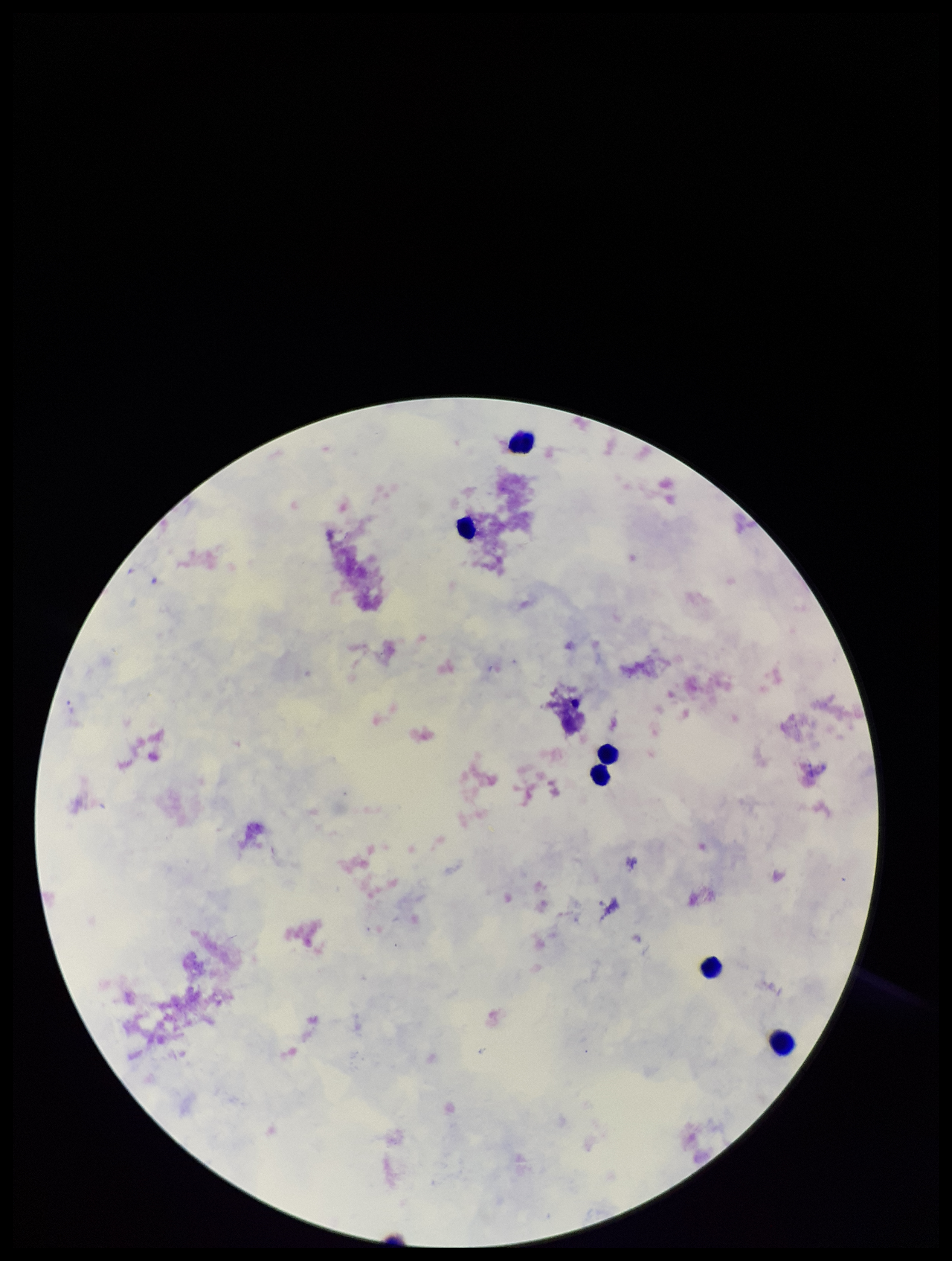
preparation = thick blood smear
parasite count = 0
image size = 952×1261 pixels
Plasmodium parasites = none seen
stain = Giemsa
leukocyte count = 6
patient malaria status = negative
field of view = one from this slide
capture = smartphone photograph through the microscope eyepiece